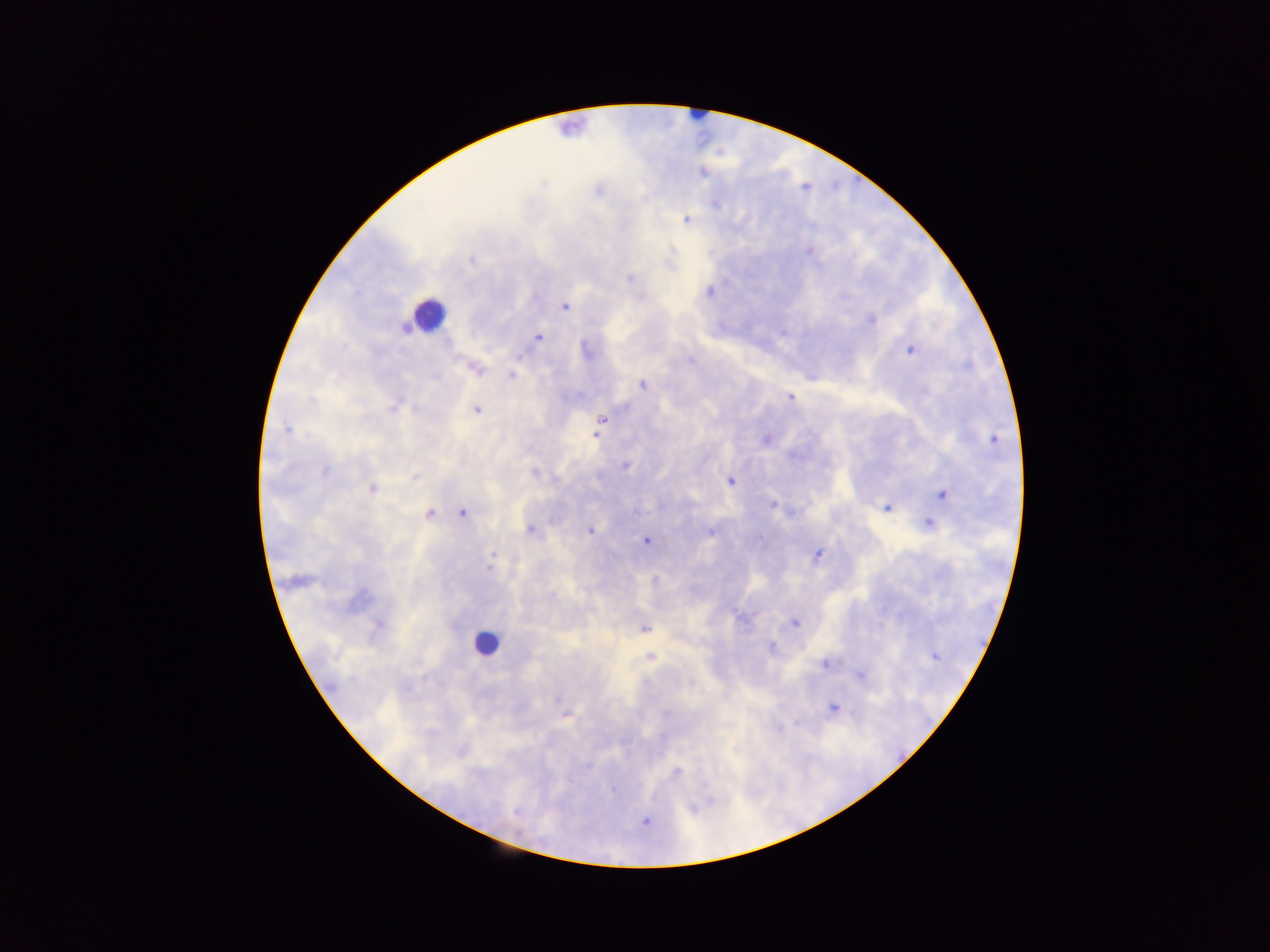

Approximate centers as (x, y) in pixels.
Summary:
  - Leukocyte locations: (428, 312), (486, 643)
  - Malaria parasite locations: (702, 173), (598, 192), (687, 220), (472, 260), (629, 277), (710, 291), (565, 306), (871, 320), (537, 336), (586, 350), (909, 350), (519, 355), (476, 369), (511, 375), (642, 384), (791, 397), (312, 402), (394, 407), (476, 409), (601, 420), (286, 429), (766, 439), (995, 440), (625, 466), (325, 471), (534, 473), (415, 477), (597, 478), (731, 481), (371, 490), (941, 495), (773, 505), (887, 508), (636, 511), (462, 513), (429, 514), (929, 524), (530, 530), (590, 531), (709, 532), (760, 538), (646, 541), (493, 556), (817, 556), (490, 562), (742, 619), (795, 622), (378, 624), (645, 628), (772, 647), (649, 656), (935, 656), (824, 664), (860, 675), (690, 683), (833, 708), (566, 715), (587, 766), (676, 771), (613, 791), (709, 802), (692, 808), (515, 812), (645, 823)
  - Field of view: single
  - Country: Ghana
  - Capture: mobile-phone photograph through a microscope
  - Image size: 1270×952 pixels
  - Preparation: thick blood smear